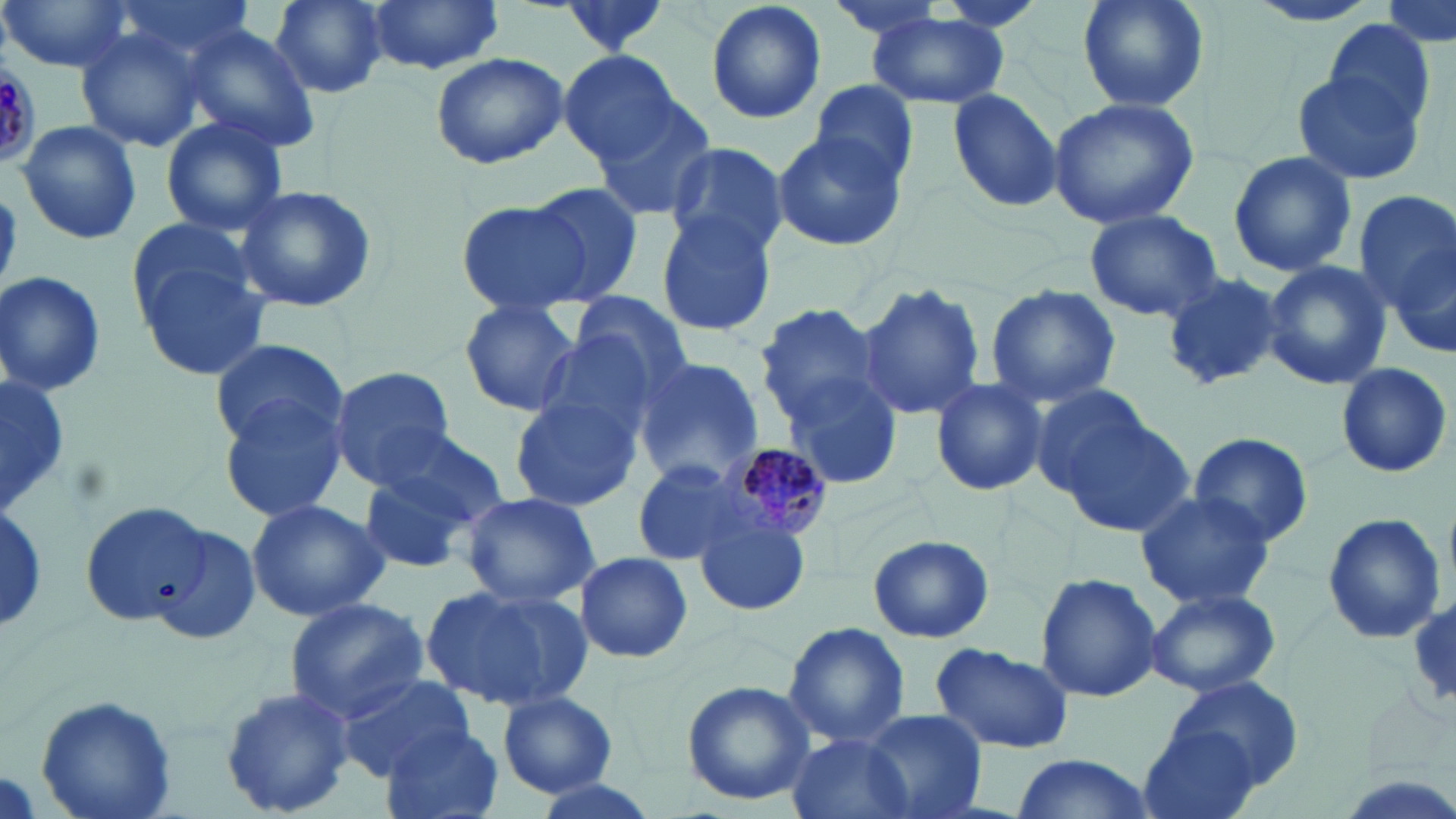

Summary:
  - Coordinate format: approximate bounding boxes as [x1, y1, x2, y2] in pixels
  - Uninfected red blood cell locations: [1, 0, 135, 74], [105, 0, 266, 71], [265, 0, 391, 98], [363, 0, 507, 76], [704, 0, 828, 124], [820, 0, 957, 41], [1075, 0, 1211, 113], [1241, 0, 1388, 29], [1380, 1, 1454, 47], [866, 11, 1012, 110], [1322, 17, 1436, 127], [179, 24, 319, 152], [75, 28, 203, 154], [559, 49, 683, 165], [429, 51, 568, 169], [2, 61, 42, 164], [1292, 69, 1426, 185], [808, 81, 919, 187], [948, 89, 1064, 212], [1047, 97, 1199, 230], [590, 98, 718, 225], [159, 116, 288, 239], [16, 120, 144, 246], [770, 128, 904, 254], [663, 143, 792, 261], [1227, 151, 1356, 279], [523, 181, 649, 306], [235, 185, 378, 314], [1352, 189, 1456, 319], [456, 197, 599, 315], [1084, 209, 1223, 323], [655, 211, 777, 339], [1379, 235, 1455, 366], [130, 237, 272, 382], [1261, 260, 1392, 392], [0, 270, 107, 395], [1159, 272, 1287, 393], [856, 281, 987, 424], [986, 283, 1122, 408], [568, 292, 692, 396], [458, 299, 584, 419], [753, 302, 887, 424], [530, 329, 670, 446], [210, 337, 349, 451], [631, 358, 766, 490], [1335, 362, 1452, 476], [327, 367, 456, 490], [781, 373, 905, 491], [930, 377, 1047, 497], [1030, 381, 1160, 506], [219, 391, 353, 521], [509, 394, 641, 512], [1051, 411, 1194, 539], [370, 425, 512, 530], [1187, 432, 1314, 549], [629, 459, 759, 566], [355, 467, 482, 575], [1135, 488, 1275, 610], [460, 491, 600, 607], [246, 497, 389, 622], [0, 500, 48, 632], [78, 502, 213, 627], [1321, 512, 1446, 646], [695, 516, 811, 618], [149, 523, 262, 647], [867, 535, 992, 643], [572, 552, 694, 664], [1034, 572, 1163, 703], [420, 582, 590, 714], [1142, 588, 1280, 698], [1408, 589, 1456, 714], [283, 596, 430, 721], [782, 623, 911, 751], [928, 644, 1075, 753], [334, 671, 474, 779], [680, 679, 816, 807], [1164, 679, 1303, 787], [219, 684, 354, 819], [34, 692, 178, 819], [496, 693, 619, 798], [858, 709, 986, 819], [1138, 725, 1266, 819], [381, 727, 505, 819], [784, 731, 915, 819], [1006, 753, 1160, 819], [522, 775, 663, 819]
  - Plasmodium malariae-infected red blood cell locations: [714, 441, 836, 549]
  - Slide-level diagnosis: Plasmodium malariae
  - Stain: May-Grünwald-Giemsa
  - Field of view: one of a larger specimen
  - Image size: 1456×819 pixels
  - Modality: optical microscopy
  - Magnification: 1000x
  - Preparation: thin blood film